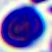
magnification = 400x
modality = photomicrograph
identification = white blood cell